Report the malaria status of this cell.
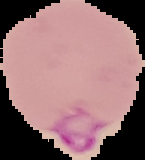

Parasitized.

image size = 145×160 pixels
image type = segmented cell region on a black background
preparation = thin blood smear